Report the malaria status of this cell.
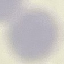
It is uninfected.

image_type: cell patch, automatically extracted from a larger field of view and resized to 64 × 64 pixels
capture: smartphone camera at the microscope eyepiece
stain: Giemsa
preparation: thin blood film